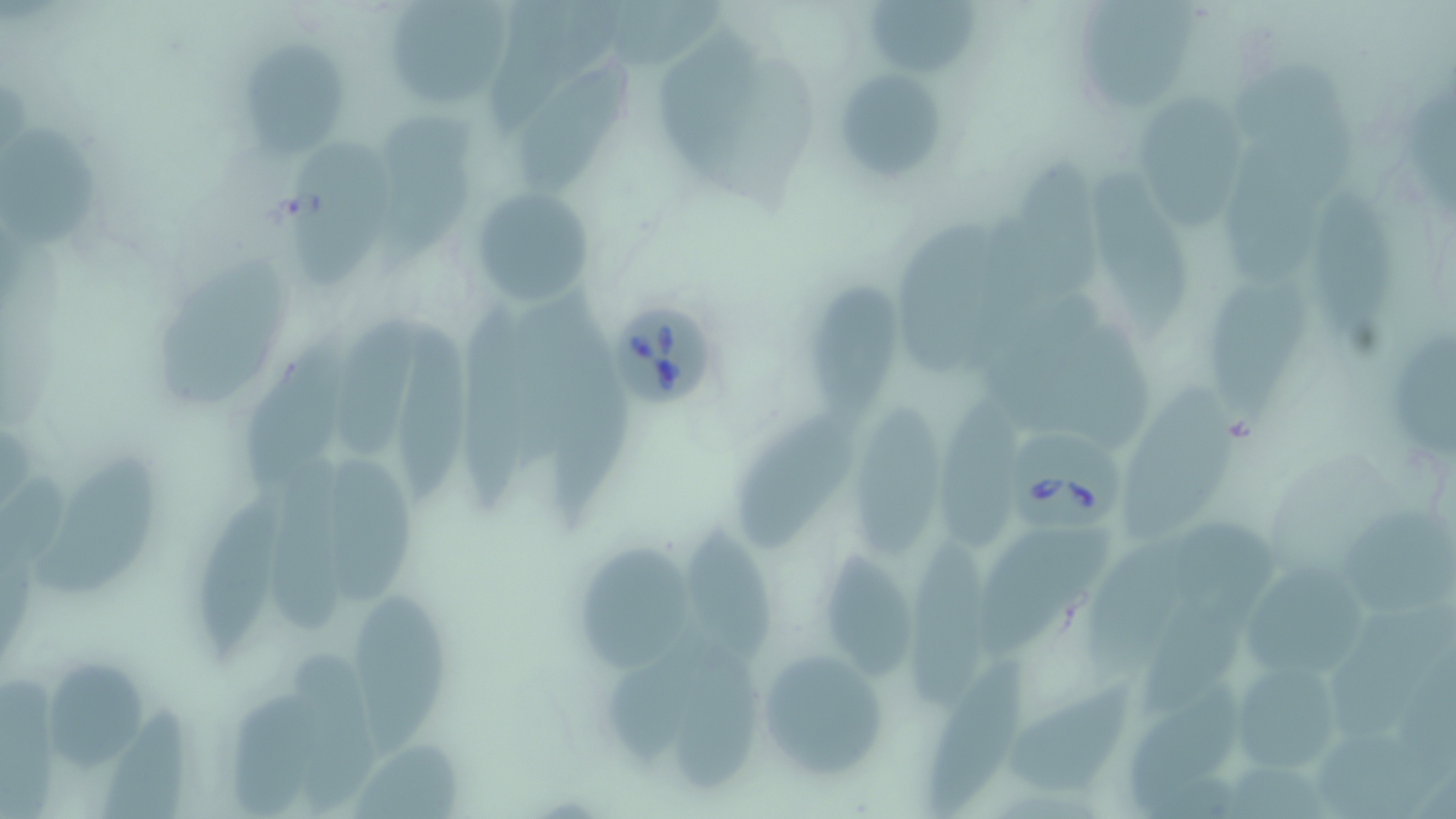 Approximate bounding boxes as named x1/y1/x2/y2 corners in pixels. Uninfected red blood cell locations: (x1=485, y1=0, x2=624, y2=138), (x1=861, y1=0, x2=987, y2=78), (x1=1077, y1=0, x2=1201, y2=110), (x1=383, y1=1, x2=515, y2=113), (x1=652, y1=26, x2=774, y2=184), (x1=236, y1=39, x2=350, y2=156), (x1=512, y1=61, x2=644, y2=196), (x1=1225, y1=64, x2=1365, y2=194), (x1=838, y1=71, x2=945, y2=182), (x1=1132, y1=93, x2=1244, y2=229), (x1=370, y1=113, x2=485, y2=264), (x1=2, y1=122, x2=105, y2=254), (x1=1225, y1=134, x2=1310, y2=290), (x1=284, y1=143, x2=396, y2=290), (x1=1009, y1=158, x2=1109, y2=310), (x1=1090, y1=166, x2=1192, y2=345), (x1=470, y1=186, x2=596, y2=307), (x1=1302, y1=186, x2=1400, y2=340), (x1=901, y1=221, x2=1003, y2=378), (x1=153, y1=254, x2=298, y2=408), (x1=1205, y1=279, x2=1320, y2=428), (x1=799, y1=280, x2=912, y2=423), (x1=454, y1=284, x2=539, y2=509), (x1=504, y1=287, x2=602, y2=472), (x1=987, y1=300, x2=1115, y2=426), (x1=345, y1=313, x2=429, y2=465), (x1=235, y1=321, x2=360, y2=506), (x1=396, y1=321, x2=484, y2=501), (x1=1388, y1=326, x2=1456, y2=462), (x1=556, y1=327, x2=634, y2=525), (x1=1070, y1=327, x2=1164, y2=456), (x1=1125, y1=387, x2=1245, y2=542), (x1=935, y1=388, x2=1029, y2=545), (x1=851, y1=401, x2=954, y2=569), (x1=737, y1=412, x2=859, y2=554), (x1=31, y1=446, x2=168, y2=601), (x1=267, y1=448, x2=373, y2=638), (x1=323, y1=448, x2=422, y2=614), (x1=196, y1=485, x2=284, y2=666), (x1=1340, y1=498, x2=1456, y2=619), (x1=1167, y1=514, x2=1285, y2=624), (x1=686, y1=526, x2=776, y2=663), (x1=977, y1=528, x2=1118, y2=664), (x1=905, y1=537, x2=1004, y2=709), (x1=580, y1=540, x2=699, y2=674), (x1=1085, y1=544, x2=1209, y2=677), (x1=822, y1=551, x2=924, y2=686), (x1=1244, y1=560, x2=1374, y2=686), (x1=1140, y1=593, x2=1244, y2=717), (x1=354, y1=597, x2=458, y2=761), (x1=1332, y1=601, x2=1456, y2=735), (x1=676, y1=642, x2=770, y2=795), (x1=617, y1=645, x2=716, y2=759), (x1=753, y1=646, x2=889, y2=782), (x1=286, y1=649, x2=378, y2=812), (x1=926, y1=654, x2=1037, y2=819), (x1=44, y1=657, x2=154, y2=775), (x1=1225, y1=658, x2=1347, y2=777), (x1=229, y1=668, x2=320, y2=819), (x1=1005, y1=676, x2=1134, y2=797), (x1=1128, y1=686, x2=1244, y2=811), (x1=93, y1=697, x2=195, y2=819), (x1=1323, y1=722, x2=1450, y2=819). Babesia divergens-infected red blood cell locations: (x1=602, y1=296, x2=724, y2=412), (x1=1019, y1=431, x2=1124, y2=537). Slide-level diagnosis: Babesia divergens. Thin blood film. Image is 1456×819 pixels. 1000x magnification. Light microscopy. May-Grünwald-Giemsa-stained preparation. One field of a larger specimen.